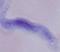 A trypanosome is seen. Micrograph. 1000x magnification.